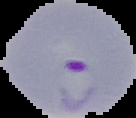
image size = 136×118 pixels
result = malaria parasites identified
image type = segmented cell region on a black background
preparation = thin blood smear